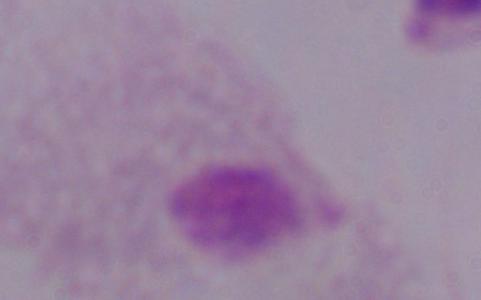

Summary:
  - Modality: photomicrograph
  - Identification: trichomonad
  - Magnification: 1000x